Comment on the morphology of the erythrocytes.
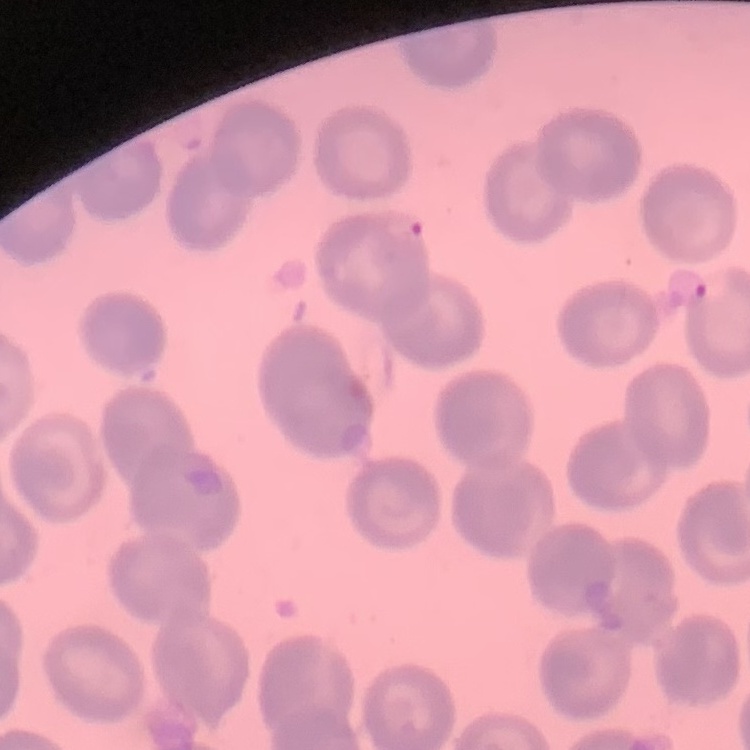
They show no rouleaux formation.

Summary:
  - Stain: Field's or Giemsa
  - Preparation: thin blood film
  - Image type: square crop of a larger photomicrograph